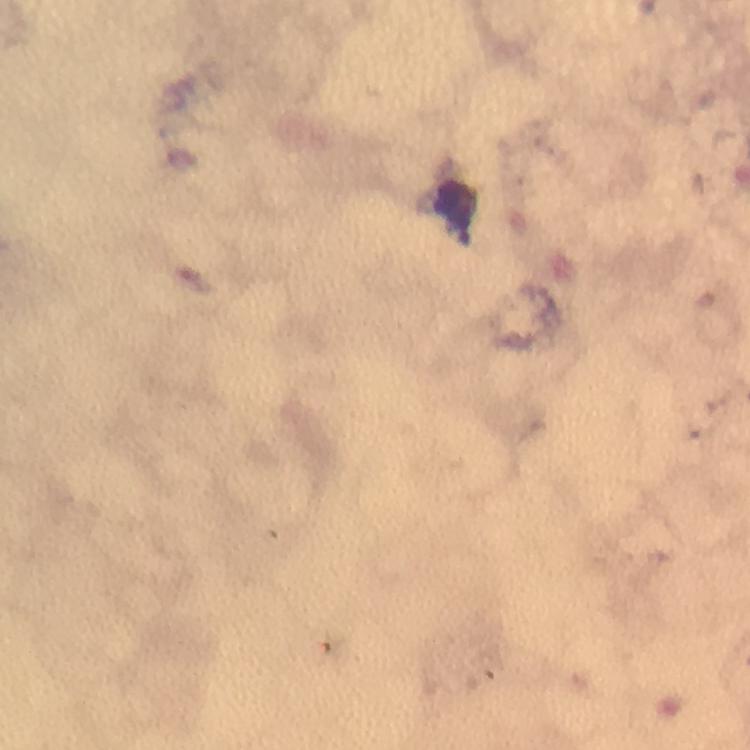
capture = smartphone photograph through a microscope
malaria parasites = none detected
magnification = 100x
cropped from = one field of view
leukocyte locations = approximate object centers, in pixels from the top-left corner: (x=458, y=209)
preparation = thick smear
stain = Giemsa
context = from a malaria diagnostic workup
immersion oil = used
image size = 750×750 pixels